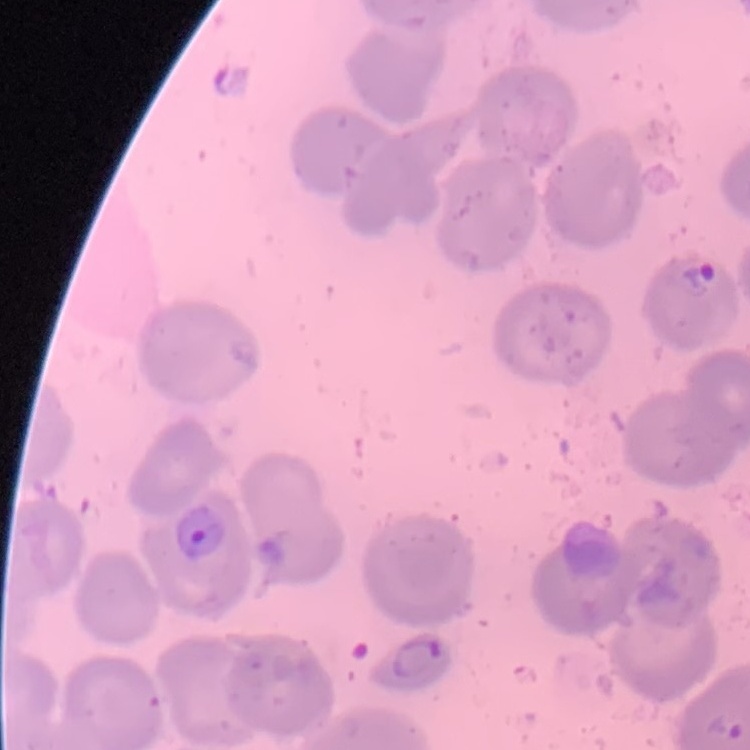

Summary:
  - Erythrocyte morphology: no rouleaux formation
  - Image type: square crop of a larger photomicrograph
  - Preparation: thin blood smear
  - Stain: Field's or Giemsa